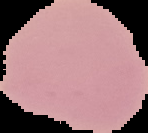
{
  "image_size": "148×133 pixels",
  "image_type": "cell region segmented out of the field of view; surrounding area masked to black",
  "malaria_status": "uninfected",
  "preparation": "thin blood smear"
}